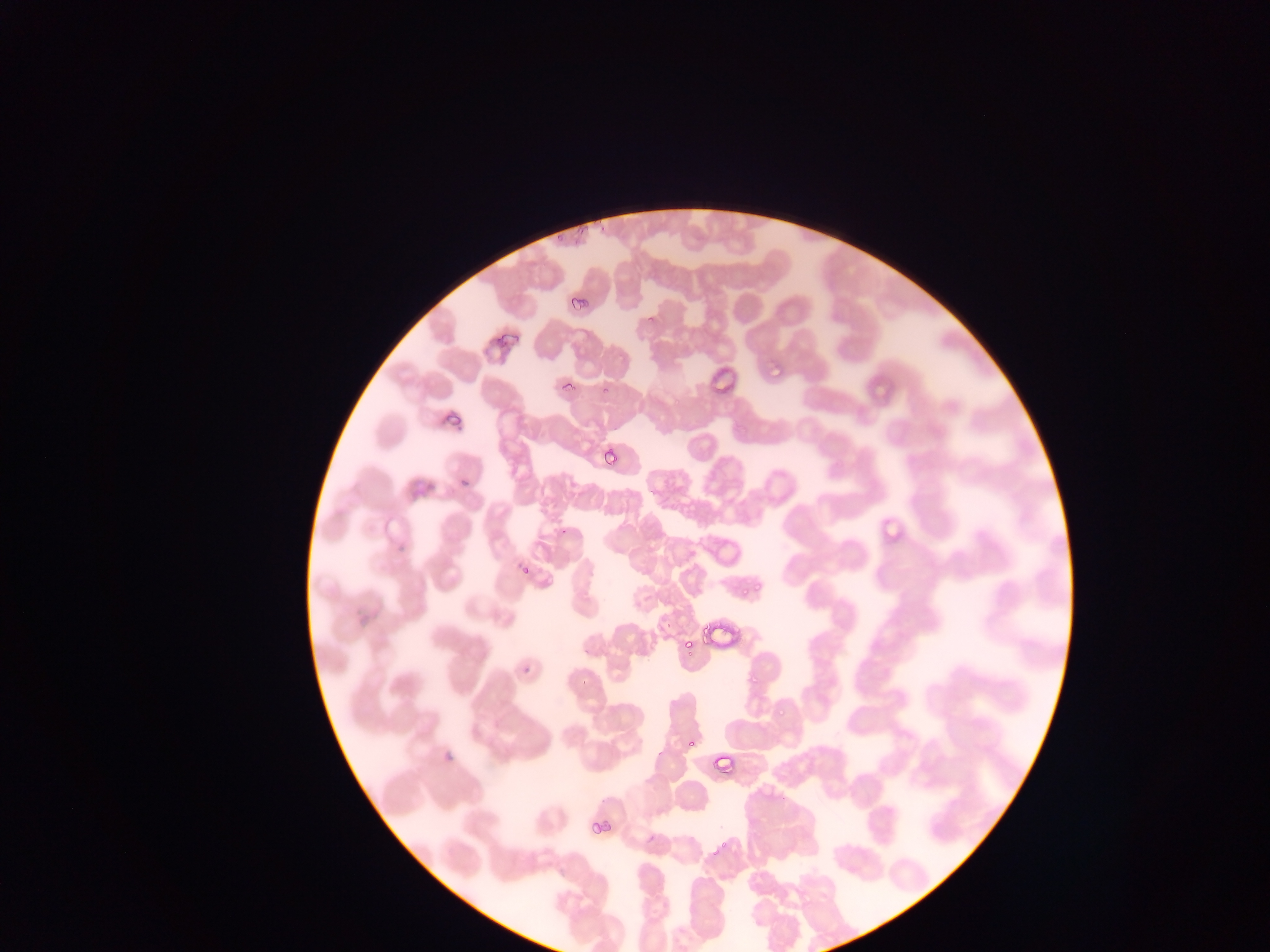
image_size: 1270×952 pixels
country: Ghana
field_of_view: single
preparation: thin blood film
malaria_parasite_locations: 'approximate bounding boxes as left top right bottom in pixels: 555 229 567 243; 580 282 590 312; 769 359 781 383; 562 379 576 392; 512 560 529 574; 753 583 764 593; 740 585 750 597; 680 628 695 648; 746 668 765 685; 779 704 787 717; 686 737 697 749; 710 751 739 783; 587 815 601 837; 601 817 616 831; 719 835 731 849'
capture: mobile-phone photograph through a microscope